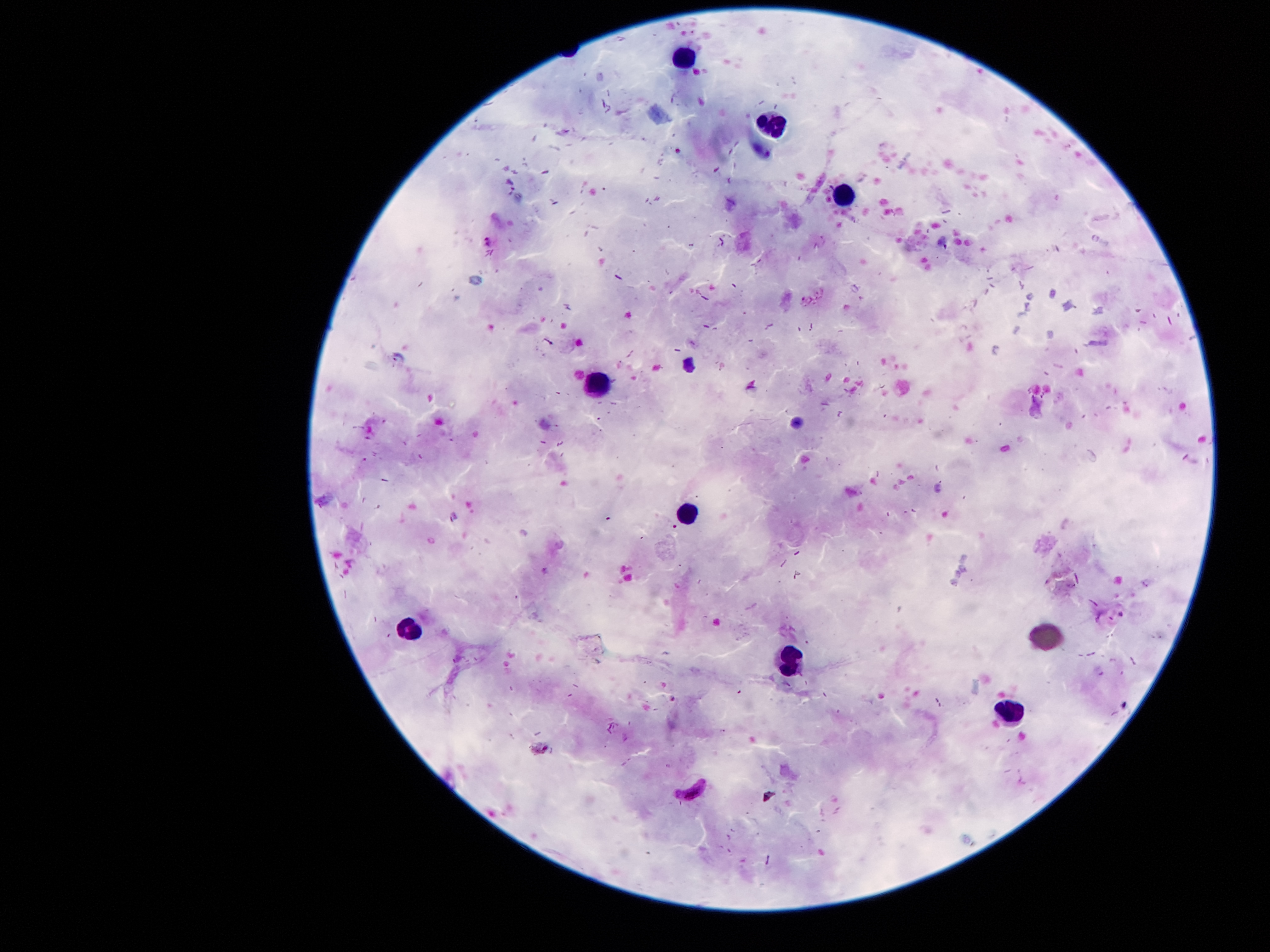 Approximate centers as {x, y} in pixels. Leukocyte locations: {680, 57}, {772, 122}, {843, 194}, {596, 380}, {683, 514}, {407, 632}, {785, 659}, {1008, 713}. Malaria parasite locations: {490, 241}, {398, 357}, {691, 792}. Smartphone photograph taken through the microscope eyepiece. 100x magnification. Image is 1270×952 pixels. Giemsa-stained preparation. One field from this slide. Thick blood film. Patient malaria status: positive for Plasmodium falciparum.